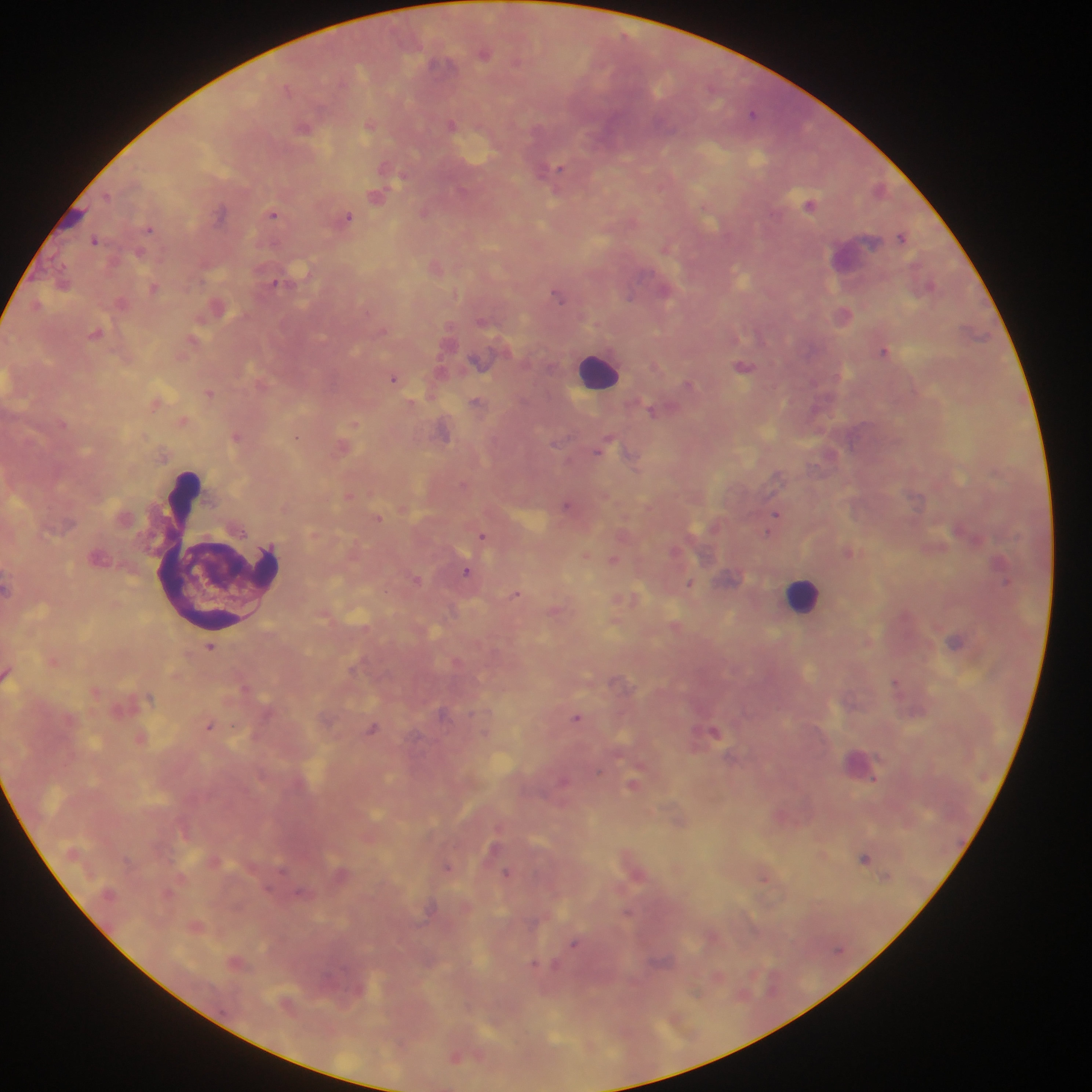

Approximate centers as {x, y} in pixels.
Summary:
  - Leukocyte locations: {598, 370}, {218, 553}, {803, 595}
  - Plasmodium parasite locations: {485, 54}, {516, 61}, {437, 64}, {287, 88}, {752, 113}, {452, 124}, {368, 125}, {303, 126}, {557, 169}, {402, 177}, {108, 196}, {377, 196}, {810, 205}, {424, 212}, {219, 213}, {272, 214}, {348, 217}, {149, 229}, {902, 236}, {94, 240}, {666, 246}, {140, 254}, {276, 282}, {154, 289}, {558, 296}, {630, 297}, {844, 315}, {884, 351}, {744, 366}, {393, 378}, {688, 384}, {211, 393}, {476, 402}, {651, 410}, {354, 425}, {237, 437}, {296, 437}, {602, 446}, {462, 484}, {566, 505}, {777, 514}, {379, 518}, {769, 532}, {482, 535}, {849, 551}, {613, 559}, {999, 562}, {467, 571}, {415, 579}, {689, 583}, {516, 594}, {956, 641}, {210, 647}, {895, 682}, {577, 717}, {209, 726}, {373, 729}, {714, 731}, {633, 784}, {865, 857}, {447, 866}, {506, 872}, {575, 944}, {535, 964}
  - Capture: mobile-phone photograph through a microscope
  - Preparation: thick blood film
  - Field of view: single
  - Image size: 1092×1092 pixels
  - Country: Ghana